Give the extent of all Plasmodium ovale-infected red blood cells.
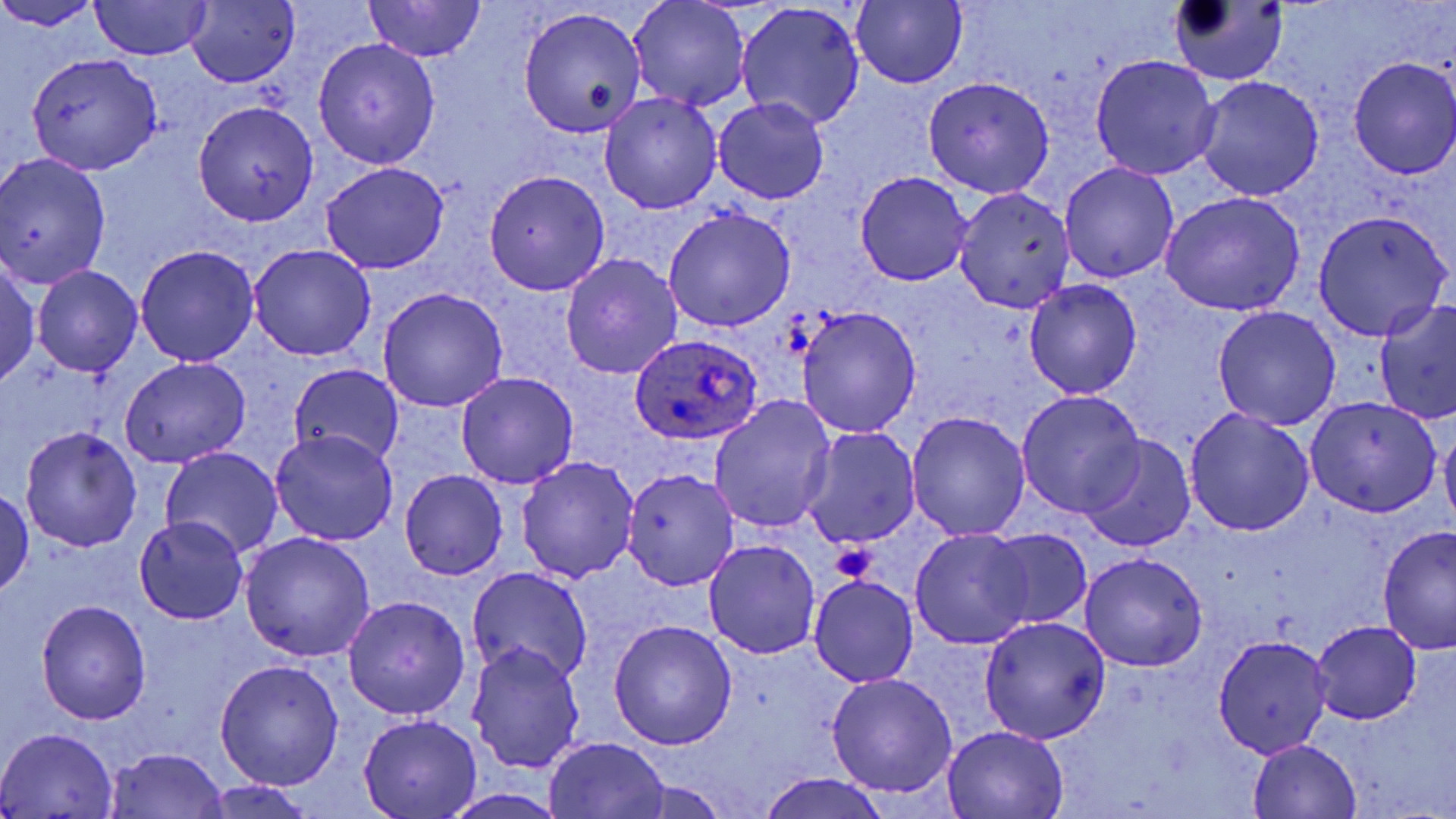
Approximate bounding boxes as [x1, y1, x2, y2] in pixels.
Plasmodium ovale-infected red blood cells: [628, 333, 763, 446].

slide_level_diagnosis: Plasmodium ovale
magnification: 1000x
field_of_view: one of a larger specimen
stain: May-Grünwald-Giemsa
platelet_locations: 'approximate bounding boxes as [x1, y1, x2, y2] in pixels: [830, 542, 876, 583]'
uninfected_red_blood_cell_locations: 'approximate bounding boxes as [x1, y1, x2, y2] in pixels: [627, 0, 749, 111], [849, 0, 970, 88], [1167, 0, 1289, 86], [89, 2, 212, 60], [365, 2, 485, 60], [0, 3, 100, 34], [185, 3, 298, 87], [736, 3, 866, 130], [519, 6, 648, 137], [312, 38, 441, 168], [26, 52, 163, 175], [1090, 55, 1221, 180], [1348, 55, 1456, 178], [1195, 75, 1325, 201], [922, 76, 1056, 198], [598, 92, 721, 215], [712, 98, 829, 205], [192, 100, 320, 225], [0, 153, 111, 290], [319, 161, 450, 273], [1060, 161, 1178, 284], [484, 171, 610, 295], [854, 172, 974, 286], [954, 188, 1075, 313], [1160, 193, 1304, 317], [662, 206, 797, 333], [1314, 211, 1451, 340], [133, 244, 260, 367], [249, 244, 377, 362], [560, 254, 682, 380], [0, 257, 41, 391], [31, 265, 143, 378], [1025, 279, 1143, 398], [378, 287, 508, 412], [1376, 299, 1456, 424], [1213, 305, 1341, 432], [798, 306, 921, 438], [121, 355, 251, 469], [291, 363, 404, 471], [455, 372, 579, 490], [1016, 390, 1146, 517], [709, 395, 837, 534], [1305, 395, 1441, 517], [1183, 408, 1315, 537], [906, 411, 1031, 541], [1440, 423, 1456, 535], [21, 426, 141, 552], [802, 426, 922, 549], [270, 429, 398, 545], [1081, 436, 1195, 551], [161, 447, 283, 560], [516, 455, 639, 583], [622, 467, 743, 592], [399, 469, 508, 578], [1, 487, 34, 597], [132, 516, 249, 623], [1377, 526, 1455, 655], [982, 527, 1094, 631], [910, 528, 1033, 650], [238, 531, 376, 663], [704, 539, 821, 658], [1079, 552, 1208, 672], [468, 566, 593, 687], [809, 574, 919, 687], [342, 595, 470, 720], [36, 599, 151, 724], [979, 615, 1112, 741], [608, 620, 738, 750], [1310, 620, 1421, 724], [1211, 634, 1332, 758], [466, 640, 586, 774], [215, 659, 344, 790], [826, 673, 957, 797], [359, 714, 482, 817], [2, 727, 118, 816], [944, 727, 1068, 817], [545, 737, 670, 818], [1248, 738, 1362, 818], [105, 748, 229, 819], [756, 771, 892, 819], [201, 781, 317, 818], [443, 790, 574, 818]'
modality: optical microscopy
image_size: 1456×819 pixels
preparation: thin blood smear